Classify this cell by malaria status.
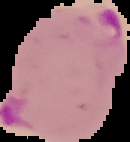
It is parasitized.

preparation = thin blood film
image type = segmented cell region on a black background
image size = 130×142 pixels